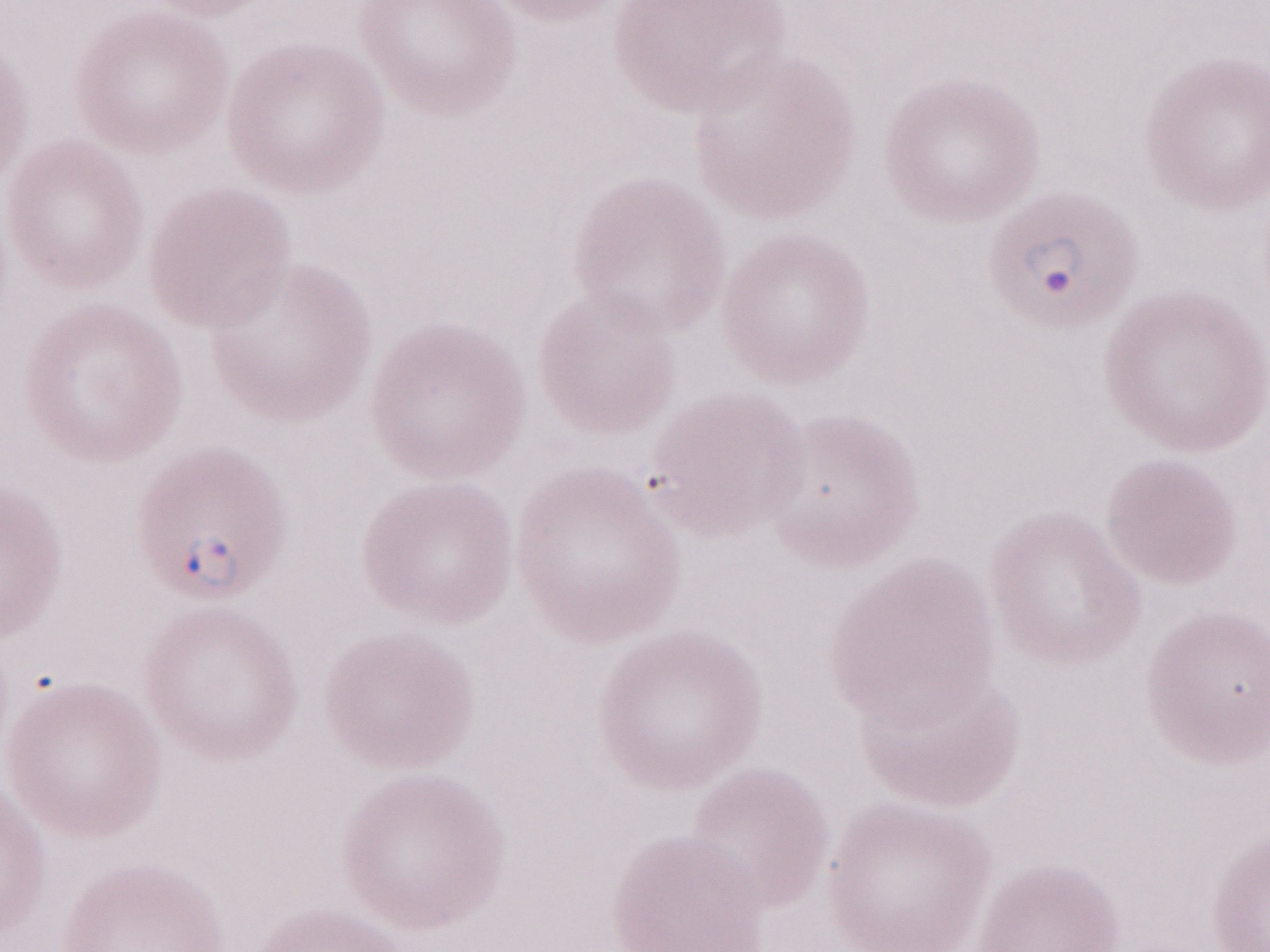
Patient-level malaria diagnosis: positive. Thin blood smear. May-Grünwald-Giemsa-stained preparation. Magnification: 1,000x. Olympus BX43 microscope and DP73 digital camera. Single field of view. Image is 1270×952 pixels.